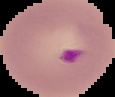

Summary:
  - Preparation: thin blood smear
  - Image type: segmented cell region with the area outside set to black
  - Malaria status: parasitized
  - Image size: 115×97 pixels